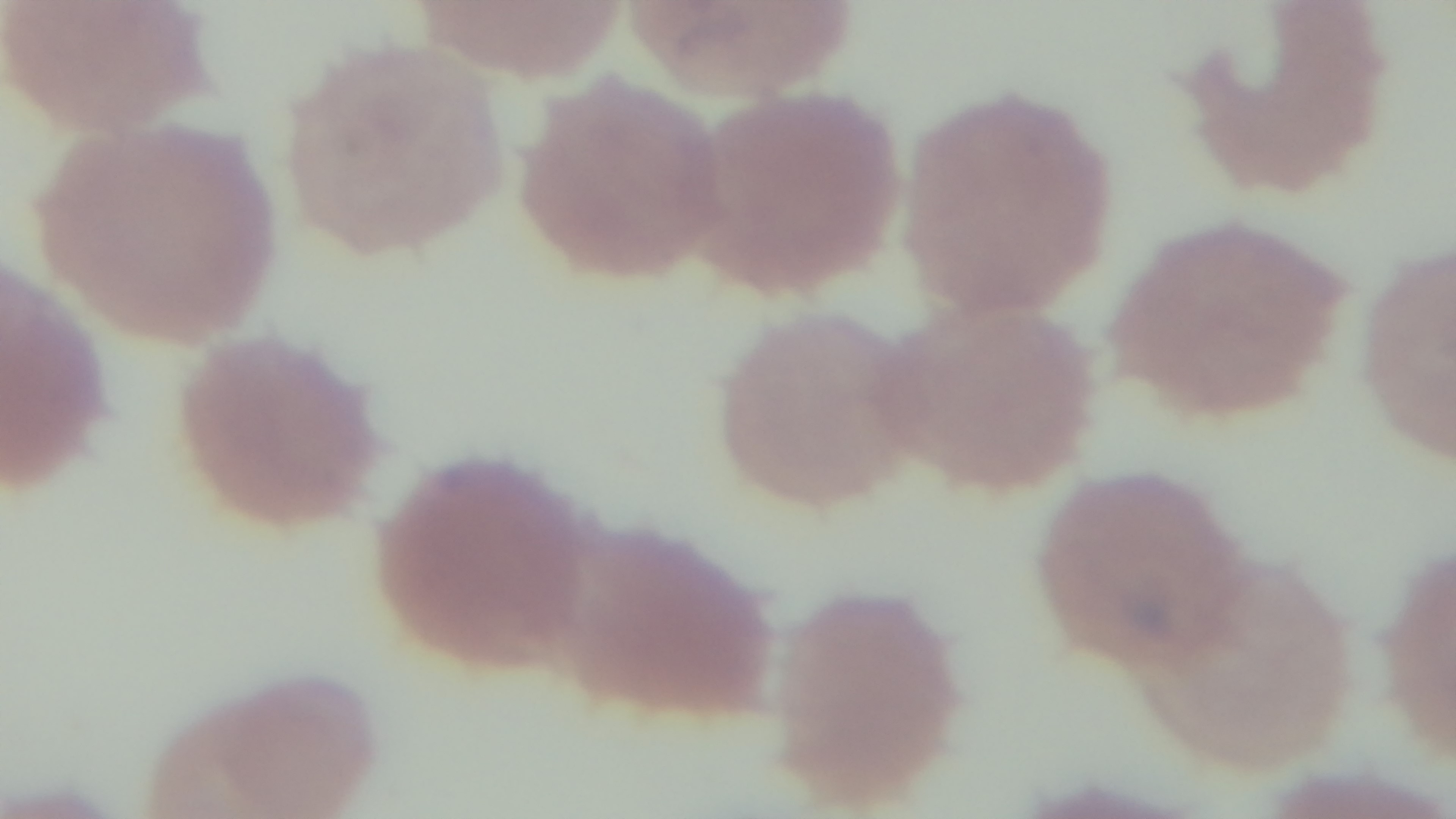

Summary:
  - Preparation: thin
  - Field of view: single
  - Capture: mounted 4K digital camera
  - Modality: light microscopy
  - Malaria status: positive
  - Stain: Giemsa
  - Objective: 100x oil immersion